Name the cell type shown.
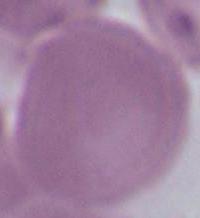
An erythrocyte.

Micrograph. Captured at 1000x magnification.